Describe the morphology of the red blood cells.
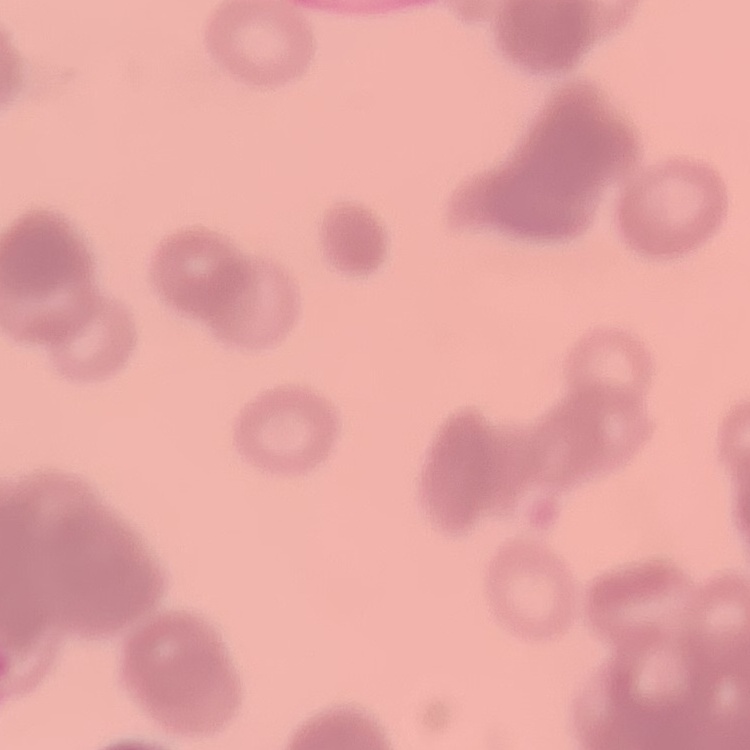
They show rouleaux formation.

Summary:
  - Preparation: thin blood film
  - Stain: Field's or Giemsa
  - Image type: one tile cut from a larger photomicrograph